Describe the morphology of the red blood cells.
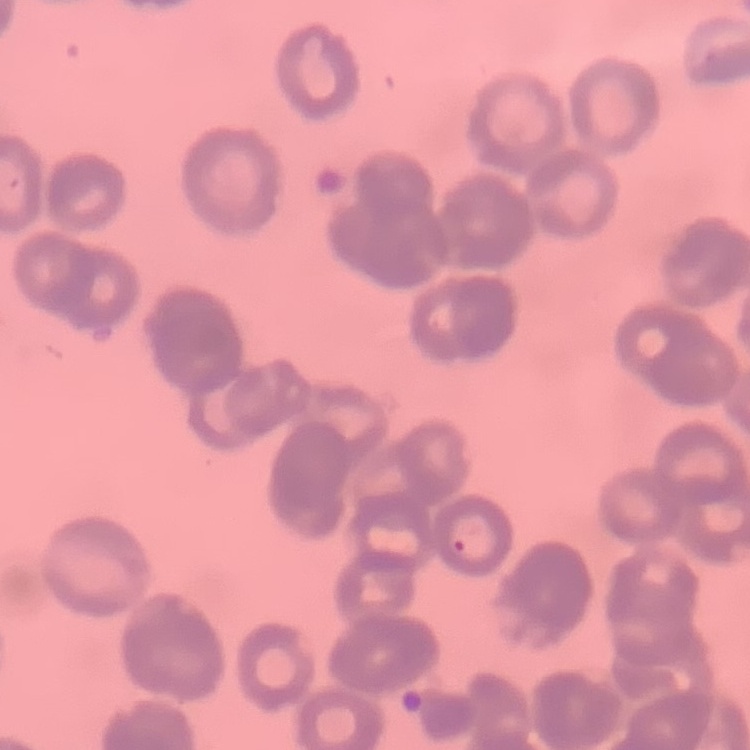
They show rouleaux formation.

Field's or Giemsa stain. One tile cut from a larger photomicrograph. Thin blood smear.